Name the parasite shown.
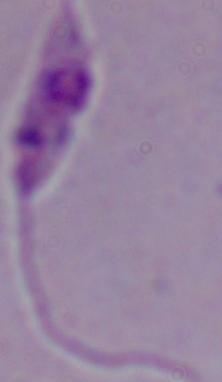

This is Leishmania.

Summary:
  - Modality: micrograph
  - Magnification: 1000x